Name the parasite shown.
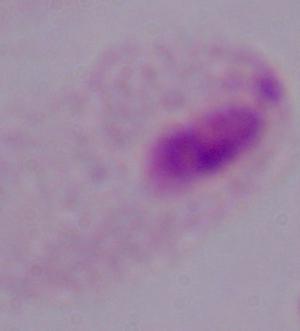

A trichomonad.

magnification = 1000x
modality = micrograph